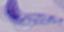

identification = trypanosome
magnification = 1000x
modality = photomicrograph